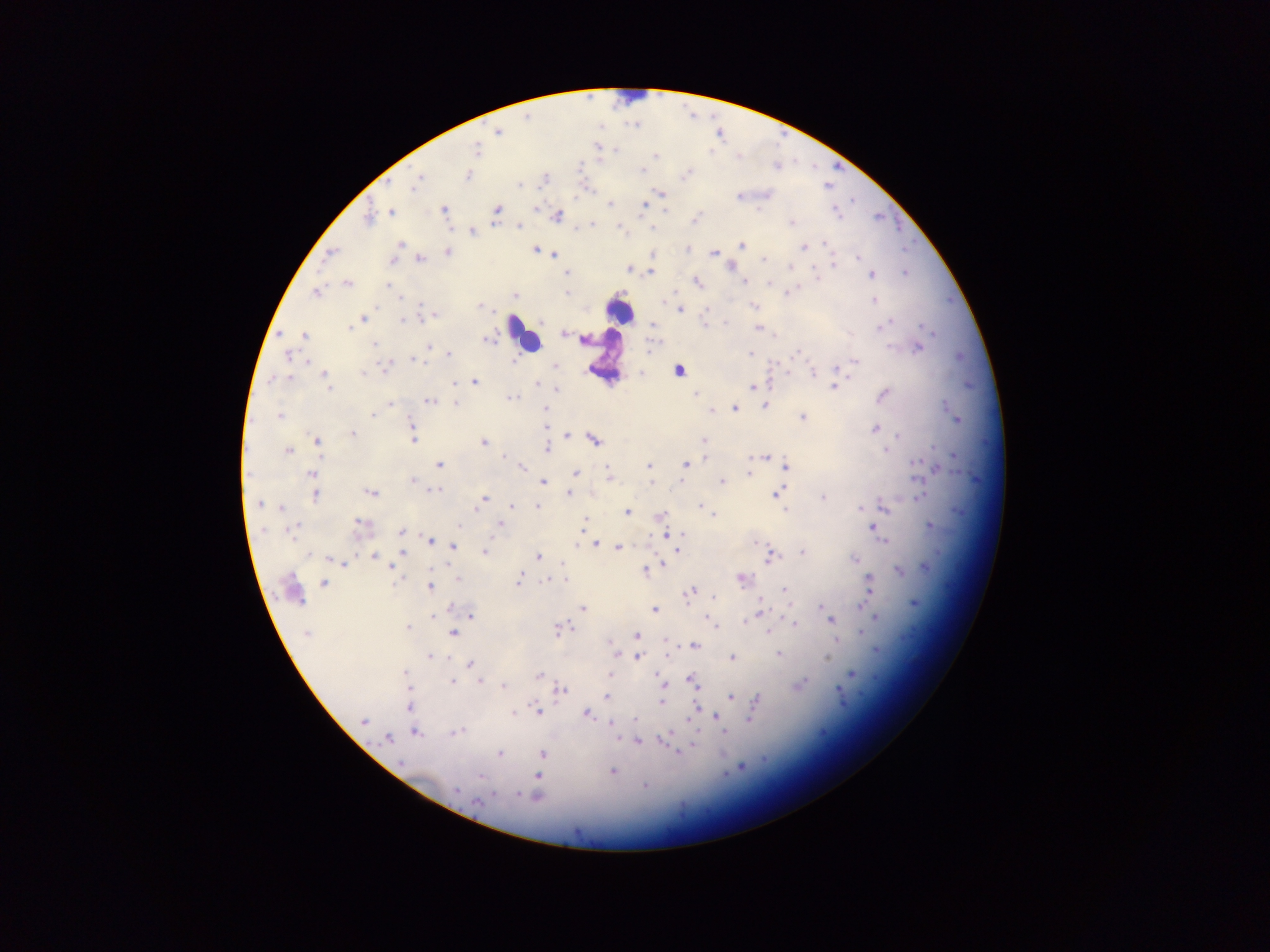

Approximate centers as [x, y] in pixels. Plasmodium parasite locations: [498, 132], [476, 150], [615, 151], [655, 156], [642, 170], [685, 175], [469, 176], [419, 177], [545, 179], [416, 182], [519, 185], [663, 194], [739, 196], [646, 202], [610, 204], [644, 205], [536, 208], [443, 209], [497, 209], [665, 211], [391, 212], [836, 213], [557, 215], [368, 218], [695, 220], [791, 223], [591, 224], [519, 227], [652, 228], [472, 232], [400, 244], [824, 244], [741, 246], [803, 247], [535, 249], [687, 250], [448, 252], [713, 253], [329, 254], [555, 255], [653, 255], [419, 258], [859, 258], [392, 260], [764, 260], [832, 263], [789, 267], [629, 269], [567, 273], [650, 273], [905, 273], [871, 274], [817, 279], [744, 281], [697, 282], [348, 284], [768, 284], [388, 285], [566, 292], [789, 292], [316, 293], [514, 296], [399, 297], [874, 300], [421, 304], [753, 305], [479, 306], [680, 310], [431, 316], [363, 318], [401, 321], [726, 323], [705, 324], [653, 325], [883, 326], [923, 326], [351, 328], [758, 328], [563, 334], [304, 335], [488, 340], [585, 340], [374, 344], [429, 346], [889, 347], [918, 349], [750, 353], [796, 353], [449, 355], [287, 356], [413, 360], [855, 361], [306, 362], [515, 362], [385, 367], [555, 367], [836, 369], [679, 371], [363, 373], [812, 373], [325, 375], [284, 379], [290, 379], [270, 381], [475, 382], [536, 384], [454, 385], [834, 387], [329, 388], [753, 388], [556, 390], [883, 394], [695, 395], [511, 397], [430, 402], [391, 404], [455, 404], [764, 405], [734, 408], [546, 410], [711, 411], [374, 414], [279, 416], [803, 416], [956, 418], [411, 425], [544, 426], [875, 428], [353, 434], [568, 435], [898, 436], [595, 439], [413, 440], [317, 441], [704, 441], [484, 443], [547, 448], [885, 450], [288, 451], [503, 457], [706, 457], [763, 458], [780, 463], [917, 463], [686, 464], [439, 465], [649, 466], [786, 466], [523, 468], [938, 468], [608, 470], [575, 473], [749, 473], [312, 474], [609, 476], [412, 480], [680, 481], [543, 482], [651, 482], [722, 482], [436, 490], [371, 493], [568, 493], [775, 493], [315, 496], [822, 497], [919, 497], [481, 502], [259, 505], [478, 505], [700, 505], [511, 506], [884, 506], [281, 507], [538, 507], [861, 508], [785, 509], [627, 512], [713, 515], [660, 516], [585, 520], [499, 523], [360, 524], [930, 525], [459, 526], [873, 527], [294, 530], [401, 531], [666, 535], [682, 535], [431, 540], [883, 540], [758, 543], [596, 545], [454, 546], [618, 548], [678, 551], [802, 552], [485, 553], [402, 554], [310, 555], [374, 556], [770, 556], [538, 557], [854, 558], [329, 559], [344, 563], [662, 563], [562, 565], [926, 566], [393, 567], [444, 567], [645, 571], [899, 572], [458, 579], [519, 579], [549, 580], [565, 580], [742, 580], [868, 580], [323, 582], [430, 587], [785, 590], [692, 592], [714, 597], [914, 603], [760, 604], [862, 605], [821, 607], [451, 608], [584, 608], [654, 610], [760, 611], [471, 615], [875, 616], [433, 617], [830, 619], [744, 621], [794, 623], [459, 627], [407, 628], [559, 629], [454, 633], [768, 633], [862, 633], [307, 634], [637, 635], [665, 643], [694, 646], [877, 650], [614, 652], [778, 654], [667, 655], [430, 656], [639, 657], [732, 657], [826, 658], [470, 664], [405, 672], [609, 674], [851, 674], [539, 676], [693, 680], [453, 681], [479, 682], [801, 683], [504, 686], [665, 686], [407, 688], [561, 690], [840, 691], [730, 697], [607, 698], [756, 701], [661, 702], [408, 706], [696, 708], [753, 708], [538, 711], [692, 712], [513, 714], [586, 714], [718, 717], [749, 718], [635, 720], [364, 721], [612, 724], [725, 731], [457, 732], [416, 733], [664, 738], [387, 739], [638, 742], [694, 743], [679, 752], [500, 753], [542, 753], [401, 763], [741, 768], [612, 771], [480, 776], [538, 776], [644, 786], [456, 790], [519, 794], [535, 795], [478, 802]. Leukocyte locations: [619, 312], [523, 333]. Collected in Ghana. Image is 1270×952 pixels. Photographed through a microscope with a mobile-phone camera. One field of view. Thick blood smear.